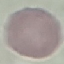
malaria status = uninfected
preparation = thin smear
image type = cell patch, automatically extracted from a larger field of view and resized to 64 × 64 pixels
stain = Giemsa
capture = smartphone camera at the microscope eyepiece